Locate every leukocyte (white blood cell).
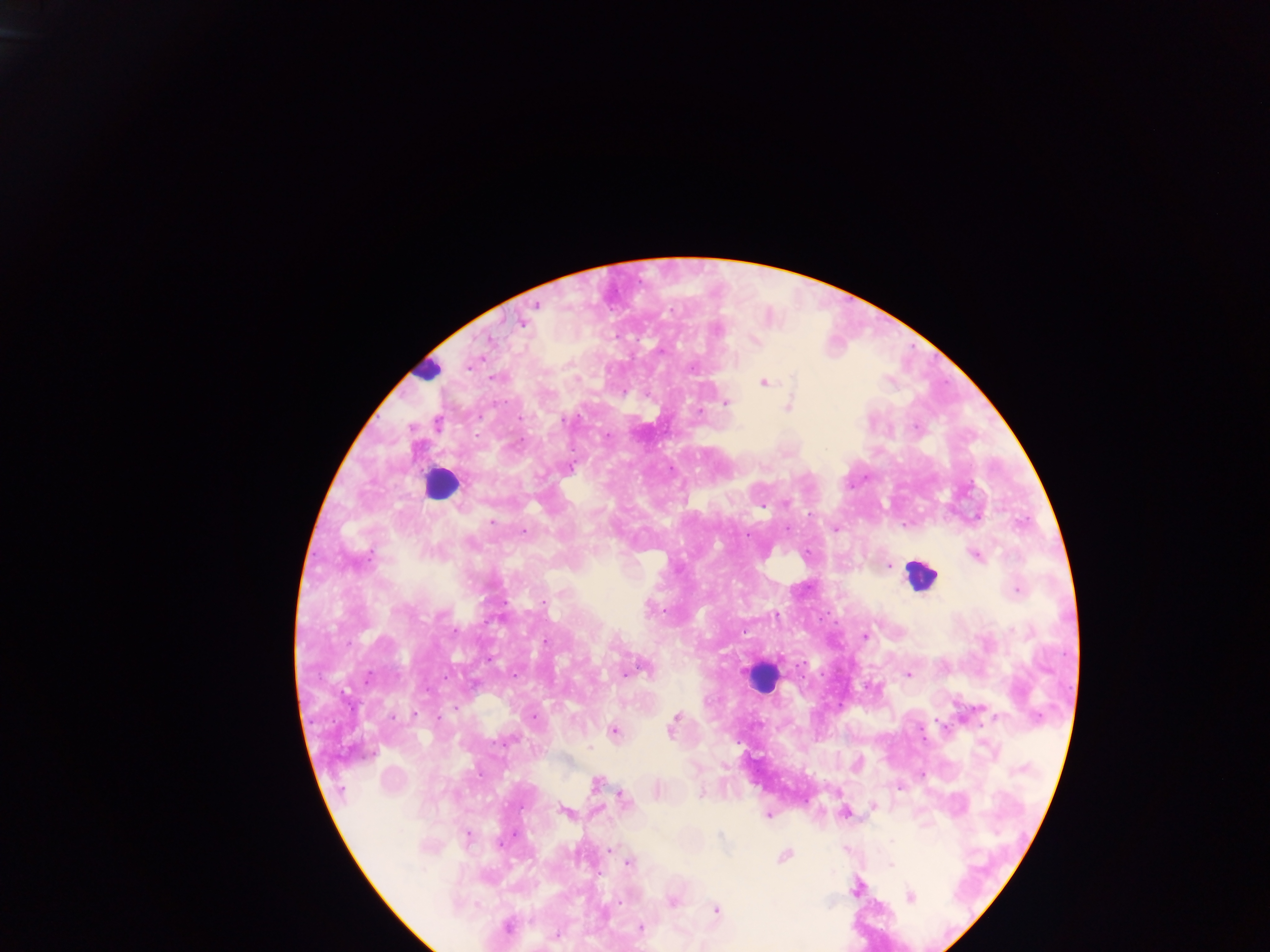
Approximate centers as (x, y) in pixels.
Leukocytes: (426, 368), (439, 484), (921, 576), (763, 676).

Malaria parasite locations: (534, 305), (520, 323), (715, 328), (488, 340), (753, 341), (660, 351), (469, 364), (692, 367), (763, 383), (725, 403), (788, 406), (698, 411), (785, 503), (976, 515), (491, 521), (835, 528), (523, 532), (975, 555), (889, 565), (1017, 590), (543, 602), (864, 636), (907, 674), (534, 716), (673, 722), (613, 732), (596, 784), (899, 787), (657, 791), (702, 793), (622, 799), (873, 806), (564, 811), (843, 812), (767, 815), (466, 837), (608, 850), (784, 856), (628, 862), (856, 888), (909, 896), (671, 901), (715, 909), (507, 926), (640, 928), (557, 934), (703, 945). Sample from Ghana. Image is 1270×952 pixels. Thick blood film. Single field of view. Photographed through a microscope with a mobile-phone camera.